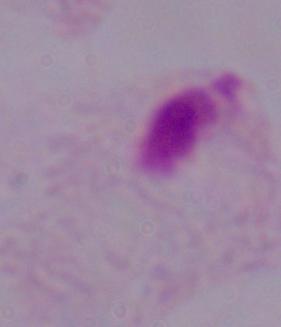
Captured at 1000x magnification. A trichomonad is shown. Micrograph.